Describe the morphology of the red blood cells.
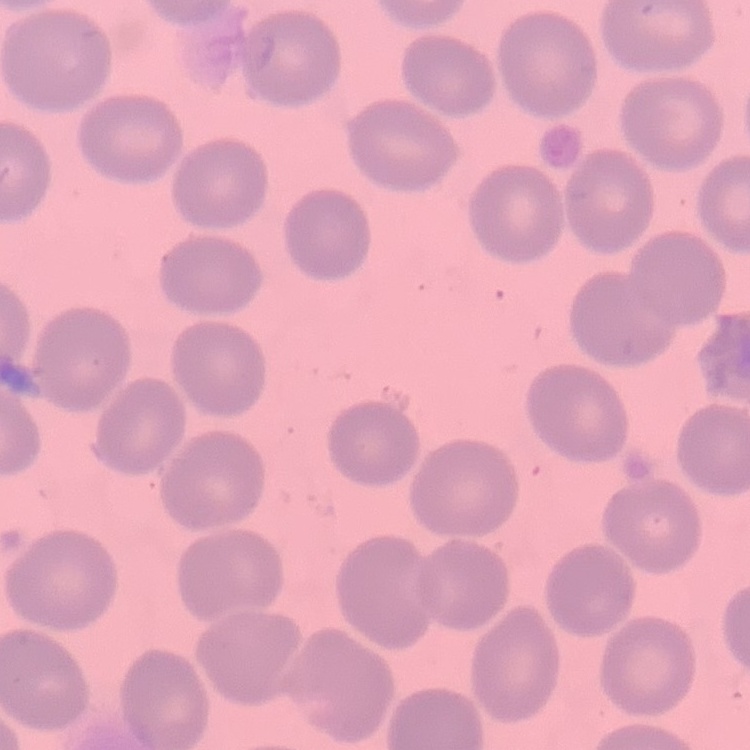

No rouleaux formation.

Thin blood film. Square crop of a larger photomicrograph. Field's or Giemsa stain.